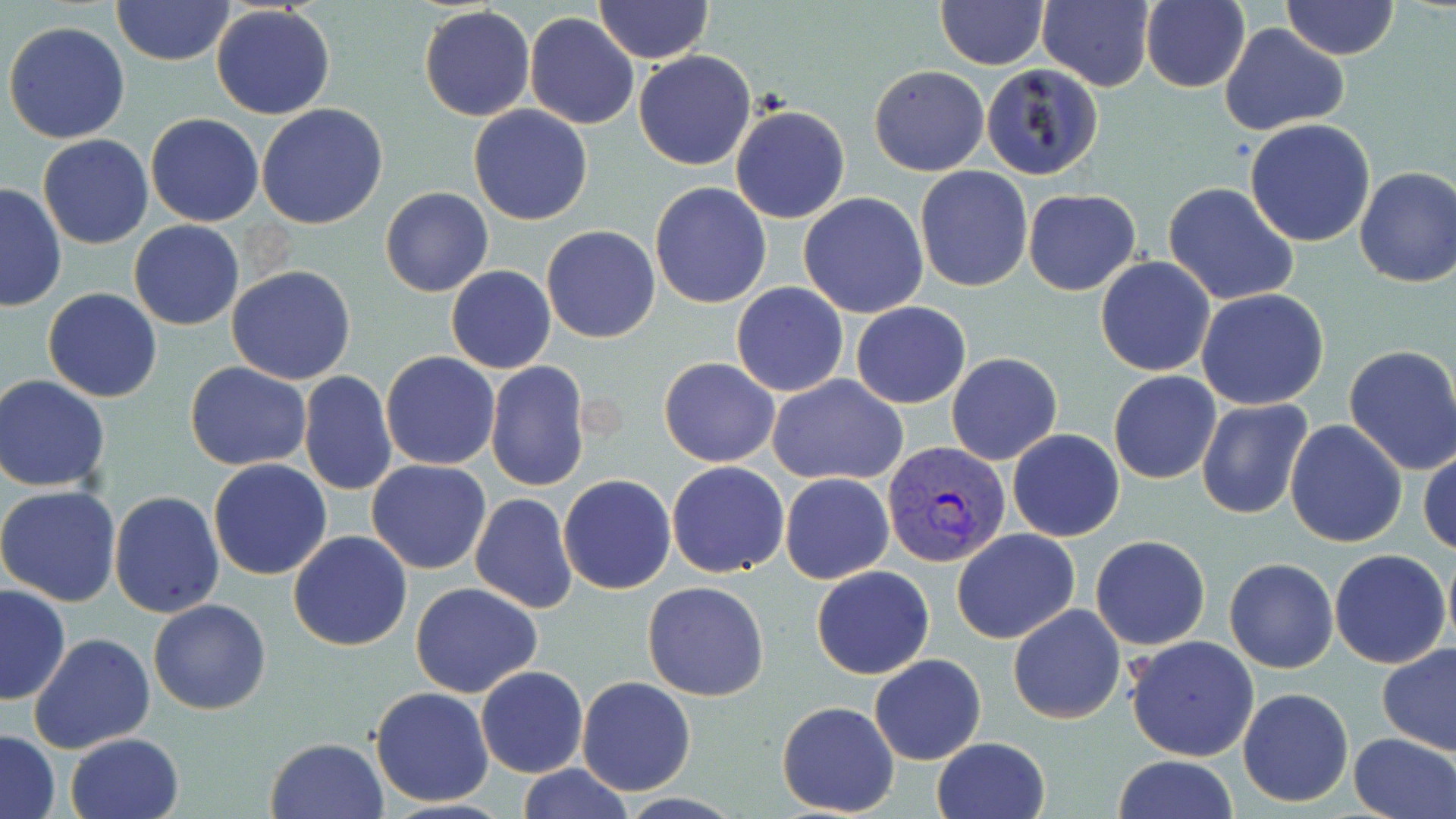 Approximate bounding boxes as (x1,y1)-(x2,y2) corner pairs in pixels. Uninfected red blood cell locations: (594,0)-(711,63), (1037,0)-(1157,92), (1140,0)-(1252,93), (1281,0)-(1399,60), (112,1)-(236,67), (936,2)-(1049,70), (211,4)-(336,121), (420,6)-(536,122), (524,12)-(639,130), (3,21)-(131,144), (1219,23)-(1349,134), (633,49)-(758,170), (980,63)-(1103,180), (869,65)-(989,175), (256,103)-(389,230), (731,104)-(850,224), (468,105)-(595,225), (145,113)-(264,226), (1244,118)-(1377,248), (37,134)-(153,249), (915,166)-(1034,293), (1354,166)-(1456,288), (649,181)-(772,310), (0,182)-(67,312), (1163,182)-(1299,306), (380,185)-(493,298), (1023,188)-(1141,295), (797,192)-(930,319), (128,220)-(244,331), (541,224)-(661,344), (1095,257)-(1216,376), (227,265)-(357,385), (446,265)-(557,374), (731,282)-(848,396), (43,288)-(163,402), (1195,289)-(1329,410), (850,301)-(971,409), (1342,344)-(1456,475), (380,350)-(501,469), (946,353)-(1062,465), (659,357)-(780,468), (485,361)-(591,491), (185,362)-(311,471), (1108,370)-(1221,484), (299,371)-(398,498), (767,374)-(908,486), (1,375)-(114,492), (1196,397)-(1314,520), (1285,419)-(1407,548), (1007,429)-(1125,542), (1419,445)-(1455,558), (208,458)-(333,580), (367,460)-(491,574), (664,461)-(790,577), (780,473)-(895,585), (557,474)-(676,595), (0,483)-(122,607), (109,491)-(225,618), (469,493)-(577,614), (951,529)-(1078,645), (287,530)-(413,651), (1090,535)-(1211,650), (1442,542)-(1455,655), (1329,549)-(1452,668), (1224,558)-(1338,672), (810,566)-(934,680), (642,581)-(769,701), (410,583)-(544,698), (0,585)-(71,705), (148,598)-(272,715), (1007,604)-(1126,723), (29,632)-(156,754), (1123,635)-(1260,760), (1378,642)-(1456,755), (869,653)-(987,765), (475,666)-(588,778), (576,677)-(696,796), (369,687)-(495,807), (1237,687)-(1355,808), (777,701)-(901,816), (1,730)-(60,817), (65,732)-(184,819), (1349,732)-(1455,818), (265,736)-(389,819), (931,736)-(1052,819), (1112,754)-(1239,818), (513,763)-(632,819). Plasmodium vivax-infected red blood cell locations: (881,439)-(1011,570). Slide-level diagnosis: Plasmodium vivax. Thin blood smear. One field of a larger specimen. Captured at 1000x magnification. May-Grünwald-Giemsa stain. Image is 1456×819 pixels. Light microscopy.